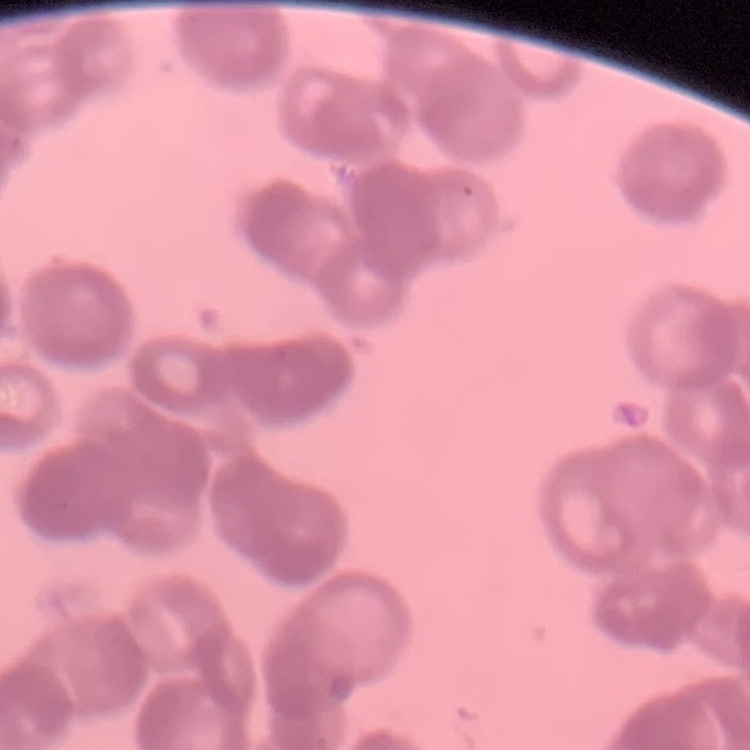
Summary:
  - Red blood cell morphology: rouleaux formation
  - Stain: Field's or Giemsa
  - Image type: one tile cut from a larger photomicrograph
  - Preparation: thin peripheral smear